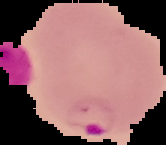
preparation = thin blood smear
image size = 166×145 pixels
image type = segmented cell region with the area outside set to black
malaria status = parasitized